Outline each Plasmodium vivax-infected red blood cell.
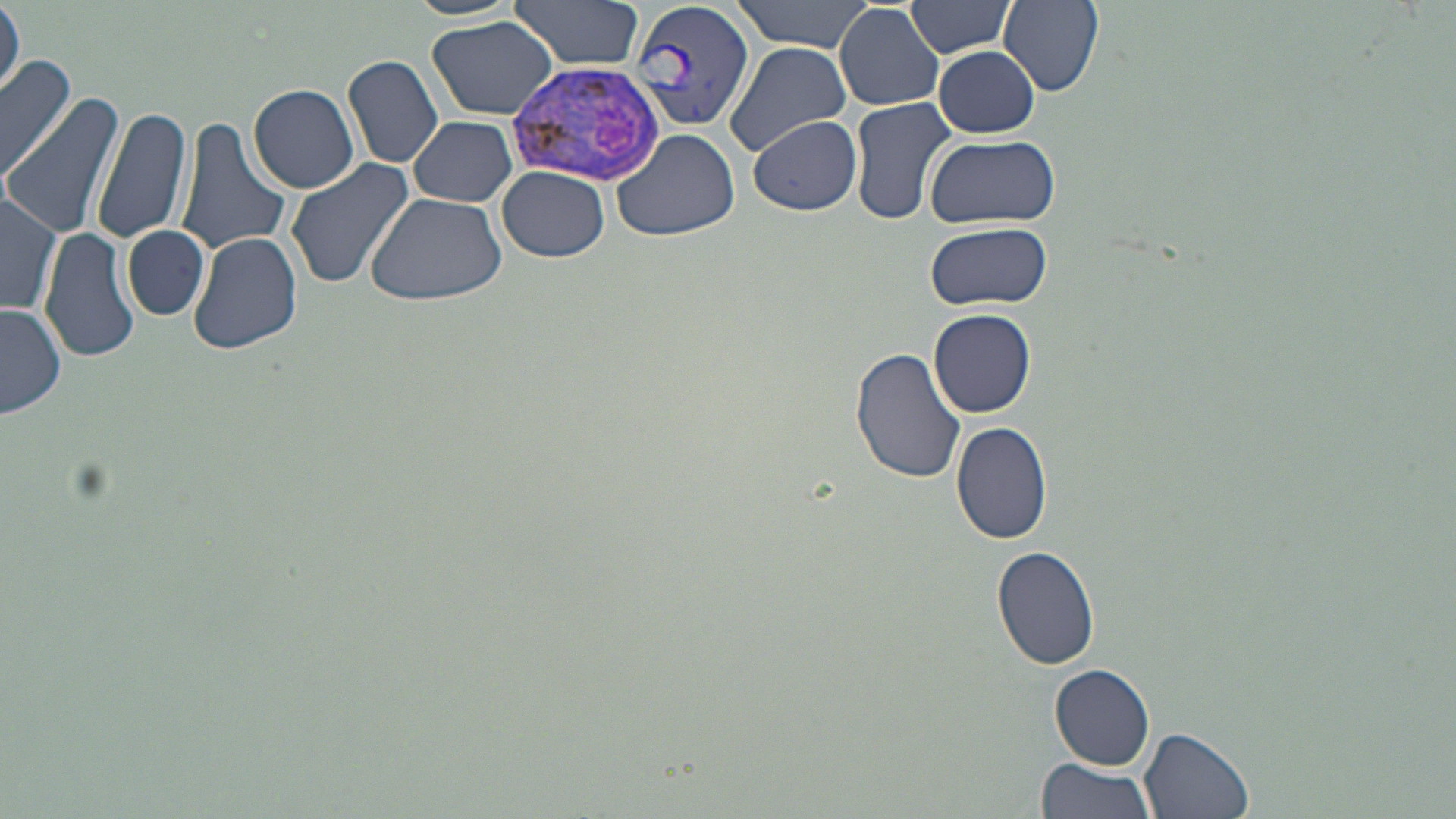
Approximate bounding boxes as [x1, y1, x2, y2] in pixels.
Plasmodium vivax-infected red blood cells: [630, 0, 754, 137], [512, 57, 667, 185].

slide_level_diagnosis: Plasmodium vivax
uninfected_red_blood_cell_locations: 'approximate bounding boxes as [x1, y1, x2, y2] in pixels: [508, 0, 645, 72], [731, 0, 880, 51], [999, 0, 1103, 96], [904, 1, 1017, 57], [2, 2, 23, 99], [834, 3, 946, 112], [427, 16, 557, 121], [724, 43, 851, 155], [933, 45, 1040, 136], [0, 53, 73, 183], [342, 55, 444, 170], [248, 83, 360, 193], [4, 95, 123, 240], [848, 97, 958, 227], [93, 102, 195, 248], [749, 114, 862, 216], [410, 116, 518, 206], [176, 118, 291, 256], [612, 127, 740, 241], [925, 132, 1059, 229], [285, 158, 415, 290], [496, 166, 610, 263], [0, 190, 62, 319], [364, 192, 509, 306], [923, 221, 1054, 311], [122, 224, 209, 322], [40, 228, 139, 364], [188, 230, 302, 355], [0, 303, 67, 419], [928, 309, 1036, 418], [851, 346, 967, 485], [951, 422, 1053, 545], [991, 543, 1101, 669], [1050, 665, 1156, 766], [1140, 727, 1256, 818], [1034, 757, 1158, 819]'
modality: light microscopy
field_of_view: one of a larger specimen
image_size: 1456×819 pixels
preparation: thin blood film
magnification: 1000x
stain: May-Grünwald-Giemsa